Classify this cell by malaria status.
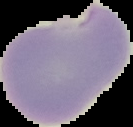
It is parasitized.

Summary:
  - Image size: 133×127 pixels
  - Image type: cell region segmented out of the field of view; surrounding area masked to black
  - Preparation: thin blood film